Comment on the morphology of the red blood cells.
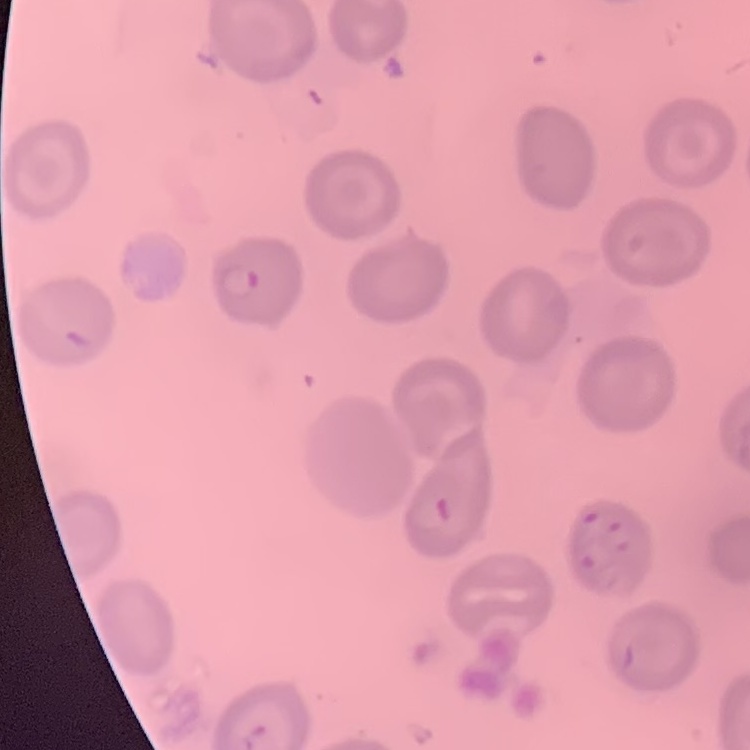

No rouleaux formation.

stain = Field's or Giemsa
image type = square crop of a larger photomicrograph
preparation = thin blood film